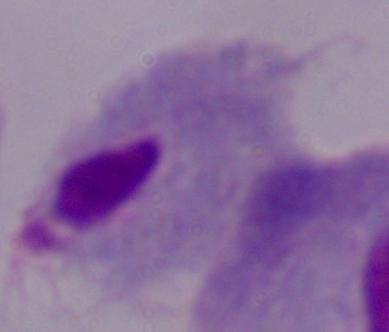 A trichomonad is seen. Micrograph. Captured at 1000x magnification.